Give the location of every white blood cell.
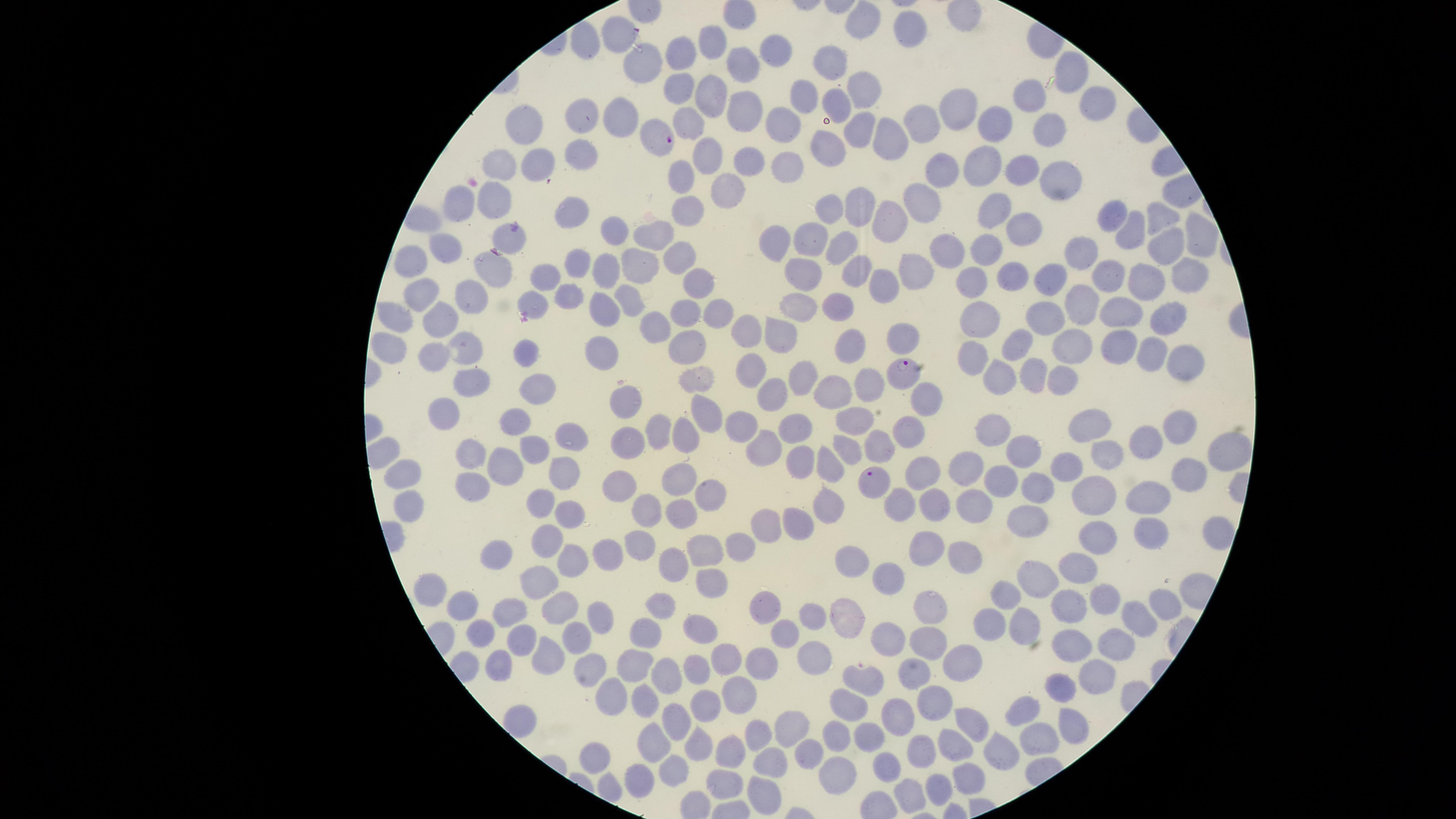

No white blood cells identified.

Approximate marker points as {x, y} in pixels. Parasitized red blood cells: {666, 140}, {900, 367}, {874, 482}. Uninfected red blood cells: {864, 21}, {910, 30}, {618, 36}, {587, 44}, {715, 44}, {774, 50}, {684, 56}, {836, 62}, {1071, 67}, {652, 69}, {744, 69}, {683, 87}, {861, 92}, {720, 94}, {801, 94}, {1026, 94}, {841, 99}, {1093, 106}, {960, 110}, {746, 111}, {584, 119}, {621, 119}, {688, 119}, {783, 123}, {920, 124}, {858, 125}, {993, 128}, {529, 132}, {1052, 132}, {885, 141}, {828, 145}, {711, 148}, {585, 156}, {747, 160}, {502, 164}, {984, 164}, {535, 167}, {783, 167}, {1019, 170}, {686, 174}, {935, 175}, {1060, 177}, {725, 190}, {495, 199}, {463, 202}, {685, 204}, {831, 206}, {918, 206}, {992, 206}, {856, 208}, {1106, 210}, {573, 212}, {1160, 214}, {883, 222}, {614, 224}, {651, 231}, {1024, 231}, {1128, 231}, {1197, 234}, {516, 238}, {806, 238}, {777, 241}, {845, 246}, {446, 248}, {1168, 249}, {989, 251}, {949, 252}, {689, 256}, {1082, 256}, {487, 264}, {579, 264}, {414, 265}, {638, 266}, {806, 269}, {854, 271}, {912, 273}, {1014, 274}, {1111, 275}, {544, 277}, {606, 277}, {1052, 277}, {1189, 277}, {977, 278}, {1150, 283}, {885, 287}, {699, 288}, {473, 294}, {430, 295}, {569, 297}, {628, 297}, {538, 299}, {1086, 302}, {799, 305}, {598, 306}, {843, 306}, {718, 310}, {1051, 310}, {687, 312}, {1118, 313}, {1165, 314}, {442, 315}, {981, 315}, {401, 319}, {654, 323}, {779, 329}, {747, 331}, {907, 331}, {849, 340}, {1018, 342}, {1072, 344}, {392, 345}, {683, 345}, {1119, 345}, {471, 349}, {532, 352}, {606, 356}, {972, 356}, {1152, 356}, {435, 360}, {1185, 364}, {749, 365}, {999, 374}, {1029, 375}, {691, 377}, {1060, 378}, {799, 381}, {868, 382}, {534, 387}, {472, 388}, {834, 390}, {766, 399}, {928, 402}, {621, 406}, {443, 414}, {515, 419}, {854, 419}, {705, 420}, {1186, 422}, {1098, 423}, {793, 428}, {744, 430}, {998, 430}, {654, 431}, {905, 437}, {686, 440}, {568, 442}, {1153, 442}, {629, 445}, {1228, 448}, {877, 449}, {1116, 449}, {529, 451}, {762, 452}, {1021, 453}, {827, 455}, {466, 456}, {852, 456}, {800, 458}, {967, 460}, {507, 464}, {1068, 470}, {681, 472}, {1189, 472}, {918, 473}, {405, 479}, {1004, 480}, {561, 483}, {618, 487}, {707, 488}, {1040, 489}, {467, 492}, {1088, 498}, {830, 500}, {539, 501}, {1149, 502}, {902, 504}, {936, 506}, {971, 506}, {679, 508}, {645, 510}, {407, 512}, {1024, 512}, {567, 514}, {765, 520}, {797, 524}, {1097, 534}, {1146, 537}, {549, 538}, {740, 545}, {638, 548}, {703, 548}, {927, 549}, {608, 551}, {962, 556}, {504, 557}, {854, 559}, {568, 562}, {674, 564}, {1083, 566}, {1036, 578}, {893, 579}, {544, 585}, {419, 590}, {704, 591}, {1006, 595}, {1107, 597}, {661, 600}, {1063, 600}, {1160, 601}, {561, 604}, {925, 605}, {461, 608}, {848, 610}, {602, 612}, {511, 613}, {1135, 616}, {812, 617}, {1028, 621}, {993, 624}, {647, 632}, {784, 632}, {701, 634}, {893, 634}, {480, 638}, {574, 639}, {931, 641}, {1068, 641}, {521, 643}, {1116, 643}, {816, 651}, {546, 652}, {727, 657}, {960, 660}, {641, 663}, {763, 663}, {502, 669}, {907, 670}, {594, 671}, {693, 673}, {665, 679}, {869, 680}, {1091, 681}, {1061, 690}, {611, 694}, {647, 695}, {743, 695}, {933, 698}, {709, 705}, {846, 705}, {1022, 707}, {891, 716}, {674, 720}, {977, 723}, {790, 728}, {1069, 728}, {870, 732}, {1038, 736}, {759, 737}, {834, 739}, {959, 748}, {700, 751}, {735, 751}, {804, 751}, {1001, 751}, {659, 752}, {924, 753}, {767, 755}, {593, 757}, {886, 766}, {671, 776}, {967, 776}, {833, 778}, {725, 781}, {936, 784}, {637, 787}, {765, 793}, {912, 794}. Photographed with a smartphone camera through the microscope eyepiece. Single field of view. Giemsa stain. Thin blood film. Image is 1456×819 pixels. Circular visible region. Presence: malaria parasites seen. Species: Plasmodium falciparum.